Name the parasite shown.
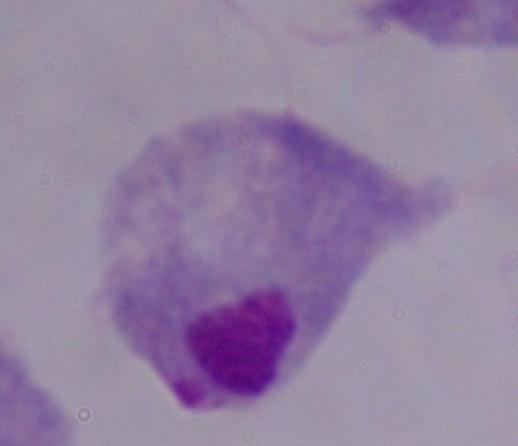
This is a trichomonad.

Summary:
  - Magnification: 1000x
  - Modality: photomicrograph